Give the position of every Plasmodium parasite.
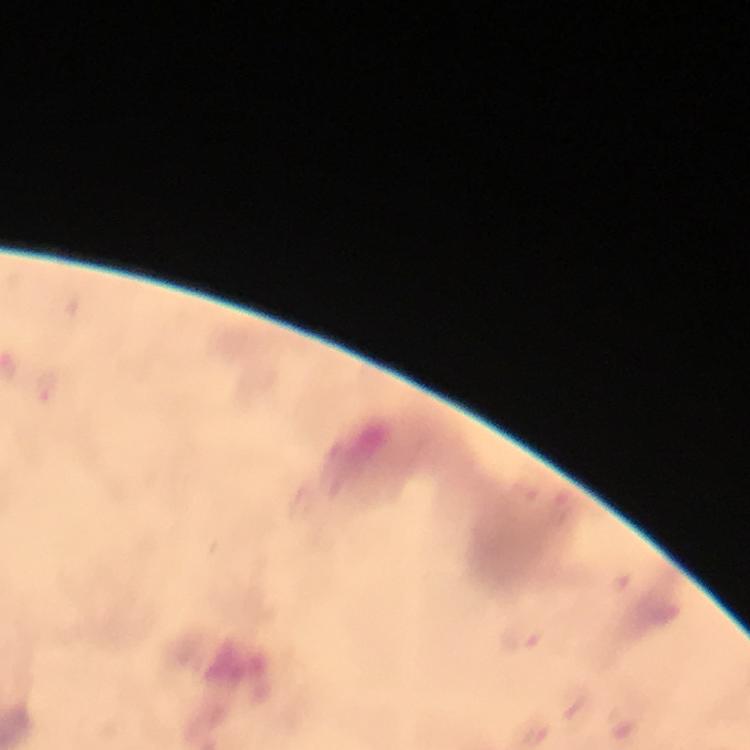

Approximate centers as {x, y} in pixels.
Plasmodium parasites: {49, 385}.

Summary:
  - Immersion oil: applied
  - Image size: 750×750 pixels
  - Preparation: thick blood smear
  - Cropped from: a single field of view
  - Capture: smartphone camera through the microscope
  - Magnification: 100x
  - Context: from a malaria diagnostic workup
  - Stain: Giemsa